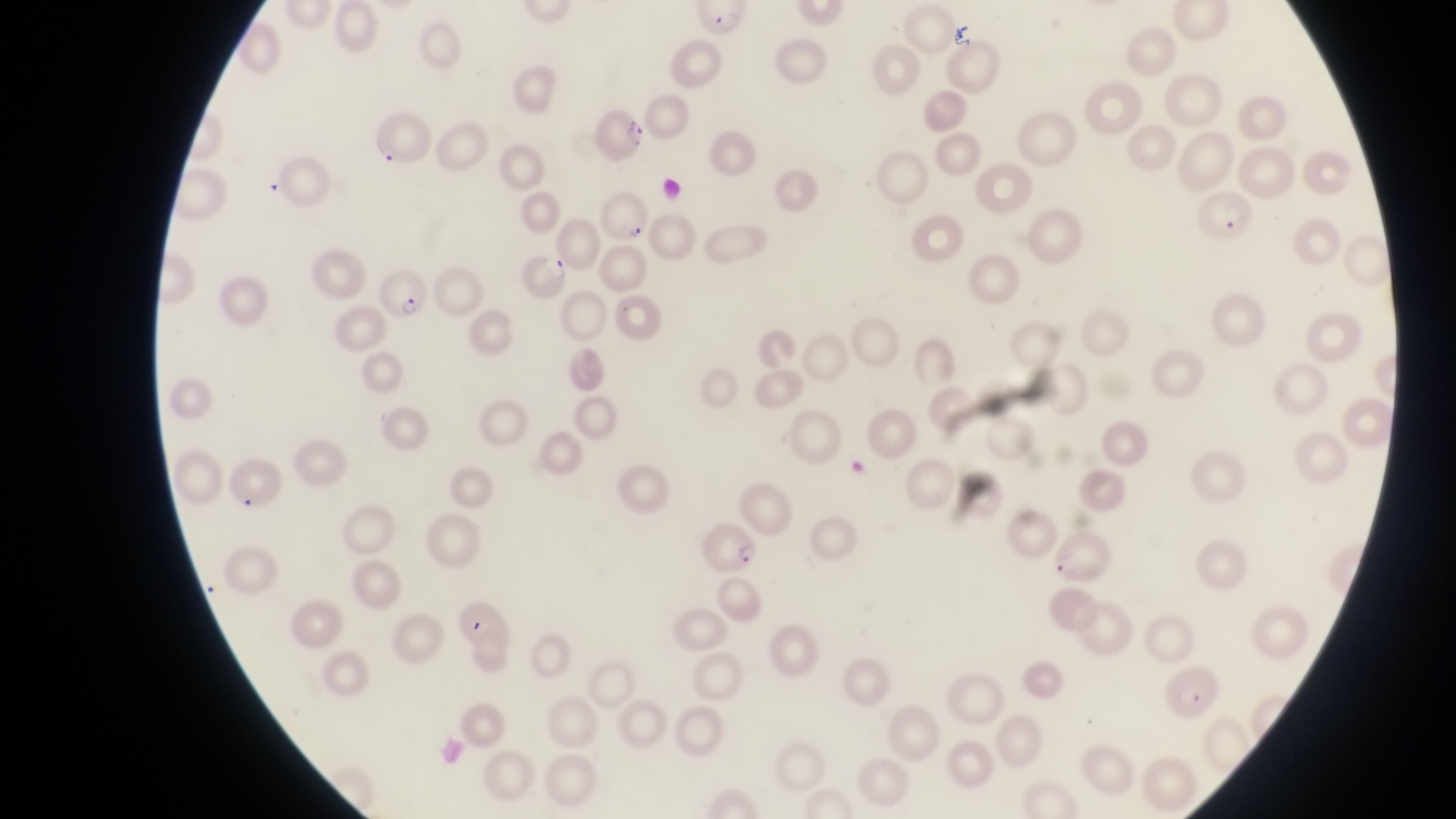
{
  "capture": "smartphone photograph through the eyepiece of an Olympus CX-23 microscope",
  "country": "Uganda",
  "preparation": "thin blood film",
  "field_of_view": "single",
  "magnification": "1000x",
  "image_size": "1456×819 pixels",
  "parasitised_red_blood_cell_locations": "approximate bounding boxes as (left, top, right, bottom) in pixels: (692, 5, 755, 38), (594, 102, 647, 155), (370, 113, 434, 166), (601, 185, 653, 248), (1203, 192, 1258, 244), (516, 254, 572, 303), (373, 265, 428, 317), (703, 521, 766, 576), (1052, 531, 1112, 590), (1159, 663, 1226, 718)"
}